Comment on the morphology of the red blood cells.
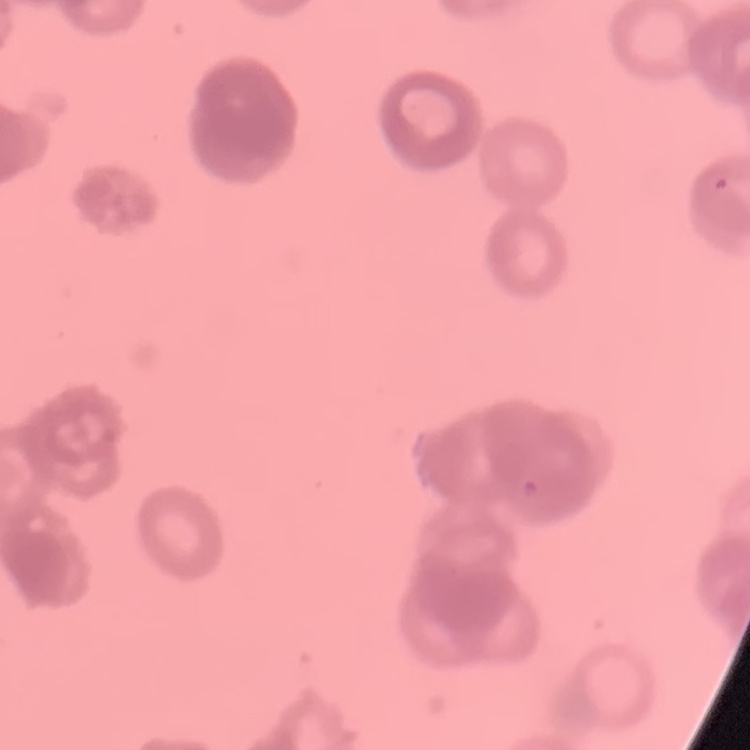
Rouleaux formation.

image_type: one tile cut from a larger photomicrograph
stain: Field's or Giemsa
preparation: thin peripheral smear